Give a bounding box for every malaria parasite, every leukocyte, and every artifact (stain precipitate or debris).
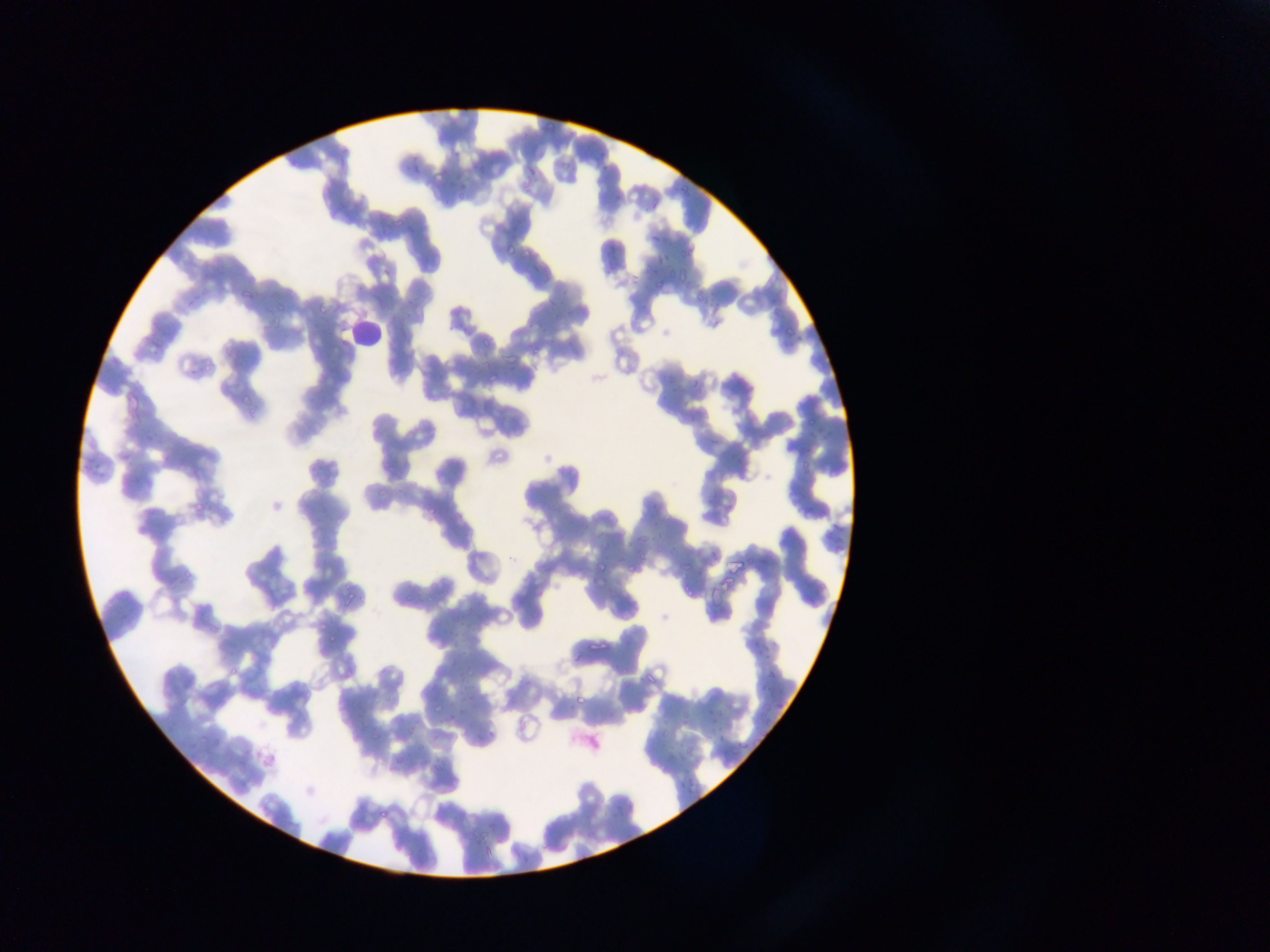
Approximate bounding boxes as (left, top, right, bottom) in pixels.
Malaria parasites: (678, 174, 707, 194), (458, 194, 464, 204), (392, 214, 408, 230), (503, 246, 518, 256), (680, 246, 692, 261), (654, 253, 670, 267), (675, 267, 692, 280), (656, 273, 667, 289), (241, 277, 264, 302), (694, 286, 709, 304), (268, 298, 289, 324), (781, 319, 808, 338), (481, 337, 491, 346), (532, 344, 549, 358), (690, 362, 716, 389), (483, 367, 501, 381), (236, 393, 254, 406), (382, 479, 398, 498), (189, 489, 215, 513), (427, 490, 453, 514), (580, 519, 594, 534), (623, 540, 634, 549), (177, 549, 220, 582), (682, 555, 705, 569), (595, 562, 603, 572), (623, 566, 637, 575), (404, 574, 426, 596), (677, 582, 695, 599), (341, 587, 363, 606), (325, 631, 344, 644), (763, 644, 780, 660), (224, 659, 246, 680), (463, 660, 481, 679), (761, 665, 786, 687), (761, 686, 780, 701), (571, 696, 581, 706), (432, 697, 446, 716), (760, 704, 775, 723), (706, 707, 715, 718), (713, 721, 729, 737), (662, 726, 677, 738), (736, 730, 752, 751), (198, 733, 207, 744), (678, 743, 698, 761), (685, 778, 698, 797).
Leukocytes: (347, 308, 394, 350).

One field of view. Sample from Ghana. Image is 1270×952 pixels. Mobile-phone photograph taken through the microscope. Thin blood film.